Locate every Babesia divergens-infected red blood cell.
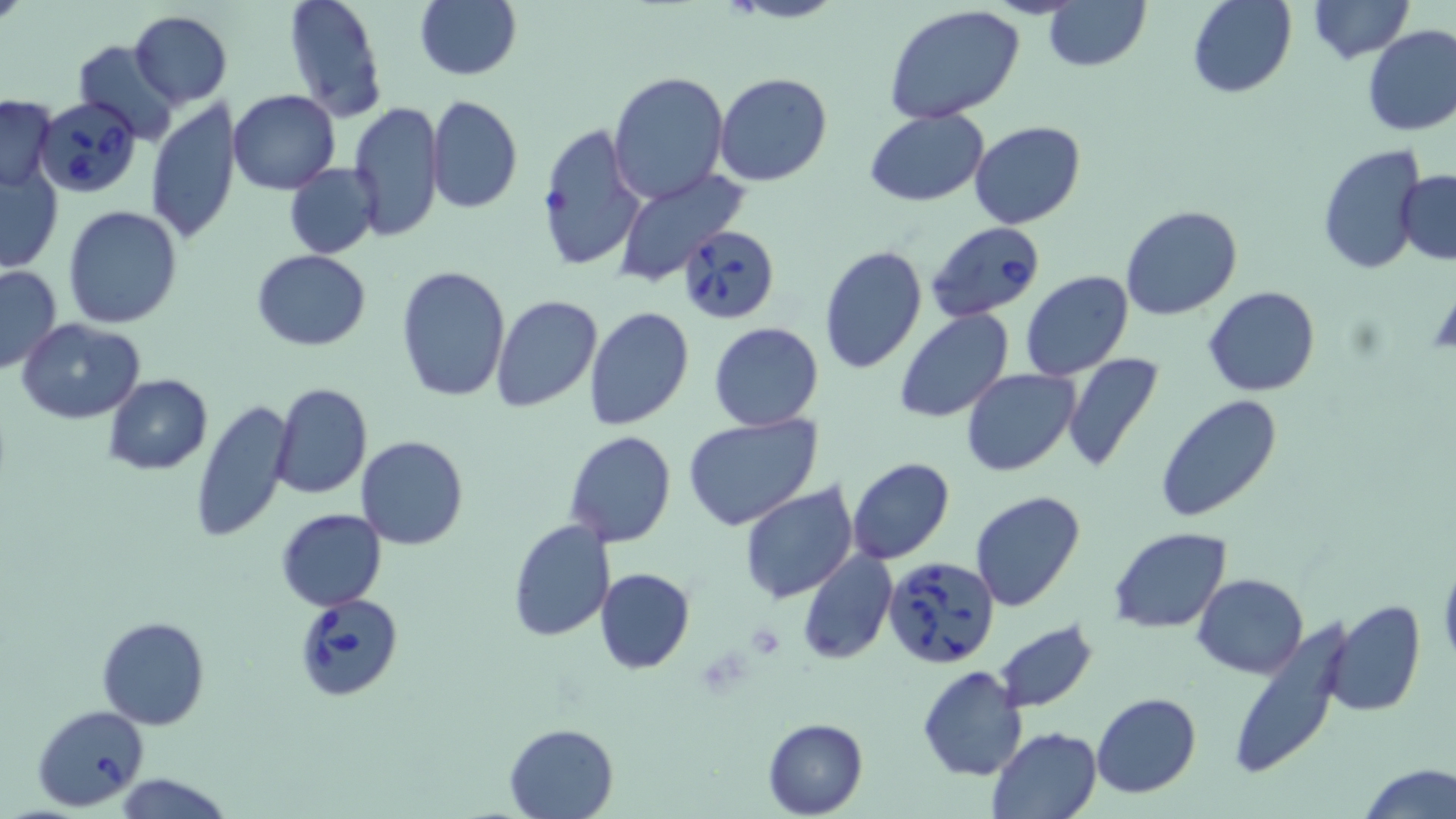
Approximate bounding boxes as (x1, y1, x2, y2) in pixels.
Babesia divergens-infected red blood cells: (36, 98, 143, 199), (927, 220, 1047, 325), (675, 224, 781, 324), (882, 555, 1000, 670), (293, 593, 404, 702), (32, 704, 152, 810).

Uninfected red blood cell locations: (1, 0, 28, 27), (283, 0, 388, 123), (414, 0, 522, 82), (715, 0, 849, 24), (1043, 0, 1151, 73), (1188, 0, 1296, 98), (1308, 0, 1412, 64), (884, 6, 1027, 127), (129, 12, 233, 107), (1360, 25, 1456, 137), (74, 40, 181, 145), (607, 71, 730, 207), (713, 71, 834, 187), (229, 90, 341, 194), (0, 94, 57, 193), (426, 94, 523, 215), (145, 97, 241, 245), (349, 101, 444, 243), (865, 108, 989, 205), (970, 121, 1086, 229), (536, 123, 646, 272), (1317, 144, 1429, 277), (284, 162, 379, 259), (0, 166, 63, 272), (612, 169, 751, 286), (1396, 170, 1456, 265), (62, 205, 185, 329), (1120, 205, 1242, 320), (819, 242, 926, 376), (250, 249, 371, 351), (0, 265, 62, 374), (395, 266, 511, 402), (1020, 270, 1135, 382), (1205, 286, 1319, 398), (490, 295, 603, 413), (584, 307, 694, 430), (892, 307, 1014, 423), (17, 318, 147, 422), (707, 321, 824, 432), (1061, 354, 1165, 472), (960, 368, 1081, 477), (102, 375, 213, 475), (270, 382, 371, 500), (1155, 394, 1283, 524), (191, 398, 294, 543), (683, 412, 824, 531), (564, 430, 677, 548), (355, 434, 470, 550), (847, 456, 955, 565), (739, 481, 858, 604), (970, 490, 1086, 611), (276, 508, 386, 611), (506, 519, 615, 641), (1108, 527, 1232, 631), (797, 549, 897, 664), (1438, 554, 1456, 669), (593, 567, 695, 674), (1193, 573, 1308, 677), (1328, 600, 1426, 718), (96, 615, 211, 730), (992, 621, 1099, 713), (1226, 621, 1353, 782), (918, 665, 1029, 783), (1092, 692, 1201, 798), (762, 718, 867, 817), (503, 722, 618, 818), (988, 726, 1102, 818), (1359, 762, 1454, 819), (114, 773, 232, 818). Platelet locations: (746, 623, 787, 658). Slide-level diagnosis: Babesia divergens. Single field of view. Captured at 1000x magnification. May-Grünwald-Giemsa stain. Optical microscopy. Image is 1456×819 pixels. Thin blood smear.